Comment on the morphology of the erythrocytes.
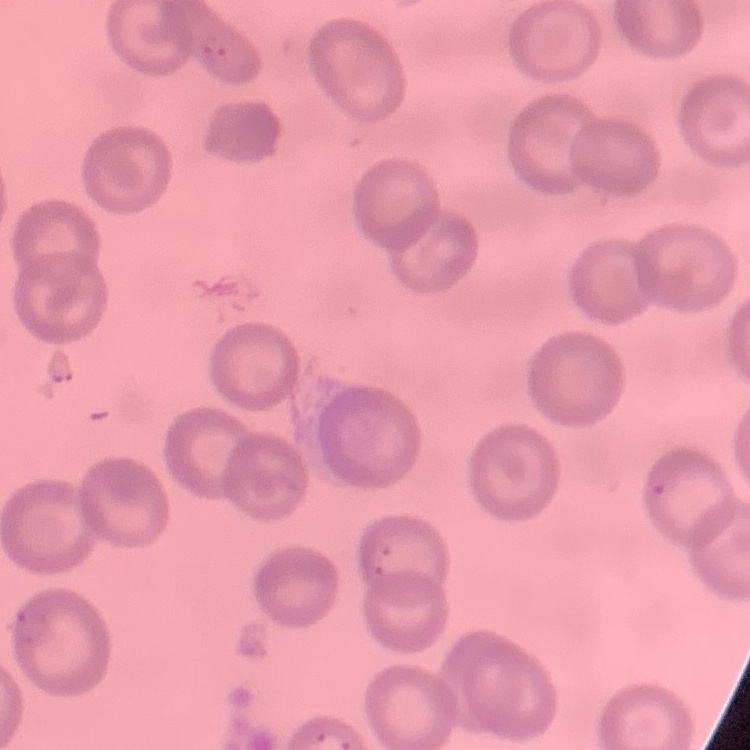
They show no rouleaux formation.

Square crop of a larger photomicrograph. Thin blood film. Stained with either Field's or Giemsa.